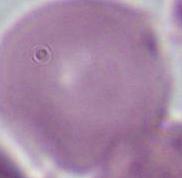

Summary:
  - Identification: erythrocyte
  - Magnification: 1000x
  - Modality: photomicrograph